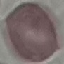
Summary:
  - Malaria status: uninfected
  - Capture: smartphone camera at the microscope eyepiece
  - Image type: cell patch, automatically extracted from a larger field of view and resized to 64 × 64 pixels
  - Stain: Giemsa
  - Preparation: thin smear